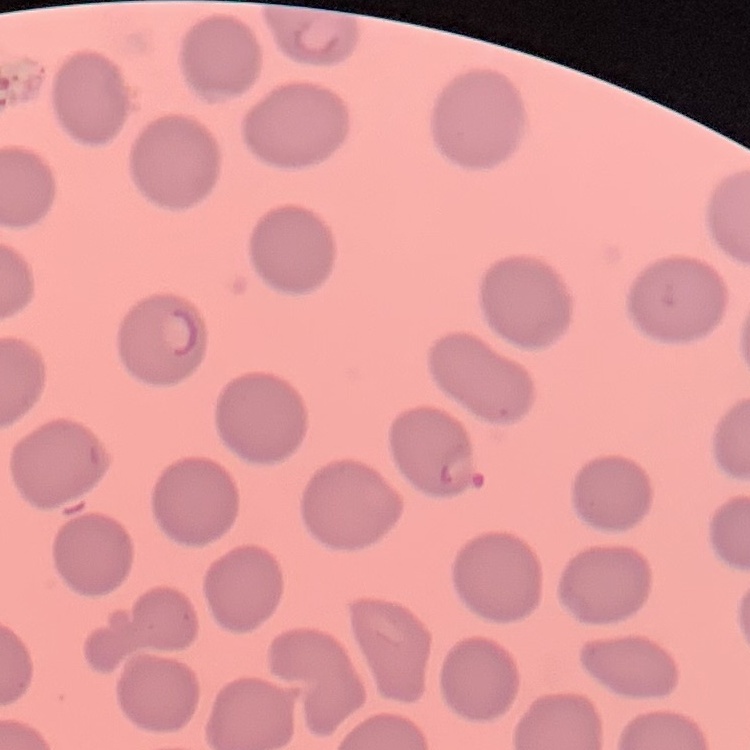

The red blood cells show no rouleaux formation. Stained with either Field's or Giemsa. Square crop of a larger photomicrograph. Thin blood film.